Comment on the morphology of the erythrocytes.
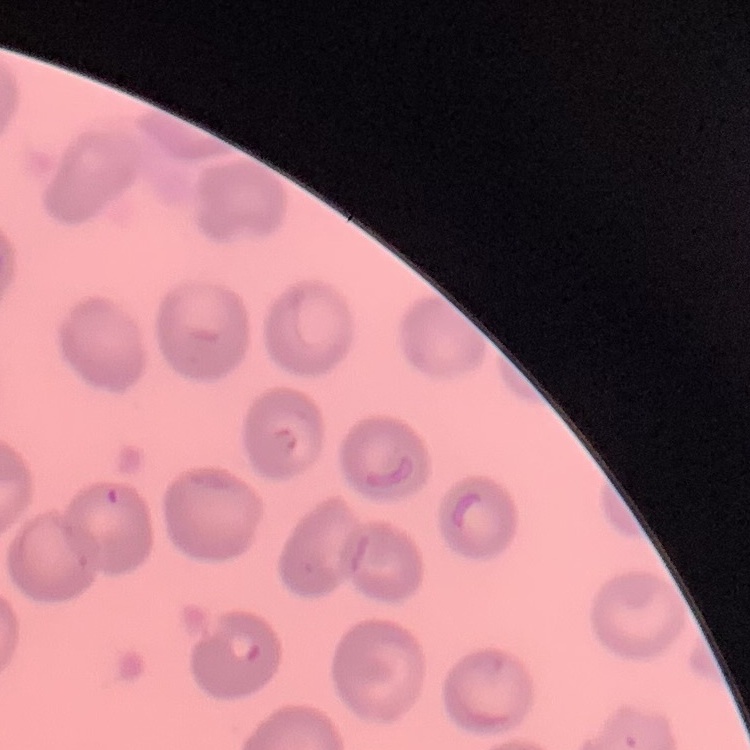

They show no rouleaux formation.

One tile cut from a larger photomicrograph. Thin blood film. Stained with either Field's or Giemsa.